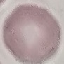

malaria status = uninfected
image type = automatically extracted cell patch, resized to 64 × 64 pixels
capture = smartphone camera at the microscope eyepiece
preparation = thin blood smear
stain = Giemsa